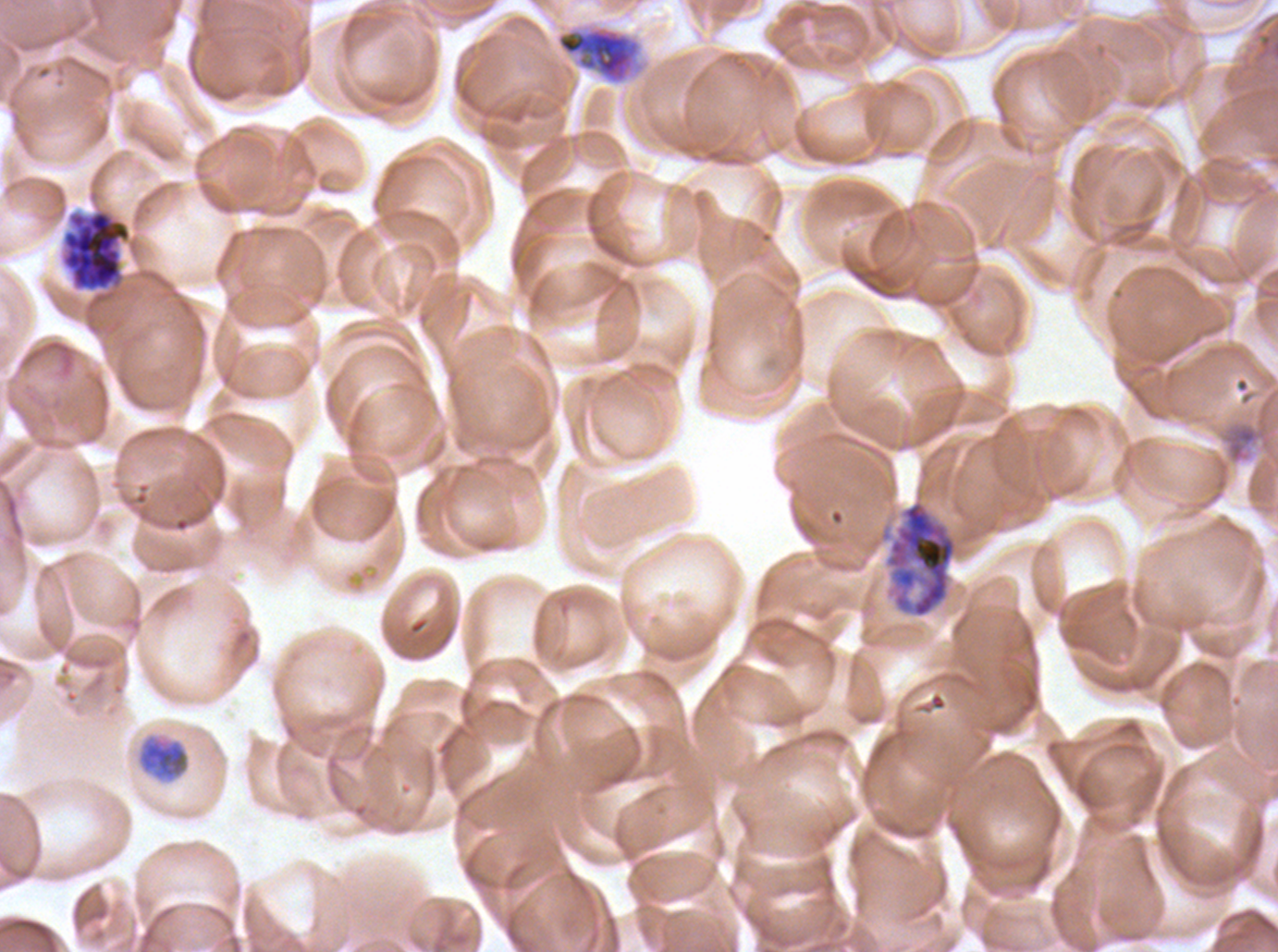
Approximate bounding boxes as [x1, y1, x2, y2] in pixels.
Summary:
  - Segmenter locations: [60, 209, 132, 292], [878, 498, 959, 619]
  - Early schizont locations: [554, 22, 647, 87]
  - Late trophozoite locations: [137, 737, 190, 782]
  - Debris locations: [1223, 422, 1271, 464]
  - Field of view: sub-image separated from a larger composite
  - Preparation: thin blood smear
  - Life-cycle stages observed: late trophozoite, early schizont, segmenter
  - Image size: 1278×952 pixels
  - Stain: Giemsa
  - Specimen: P. falciparum from a patient in The Gambia, cultured ex vivo for 24 to 48 hours